Comment on the morphology of the red blood cells.
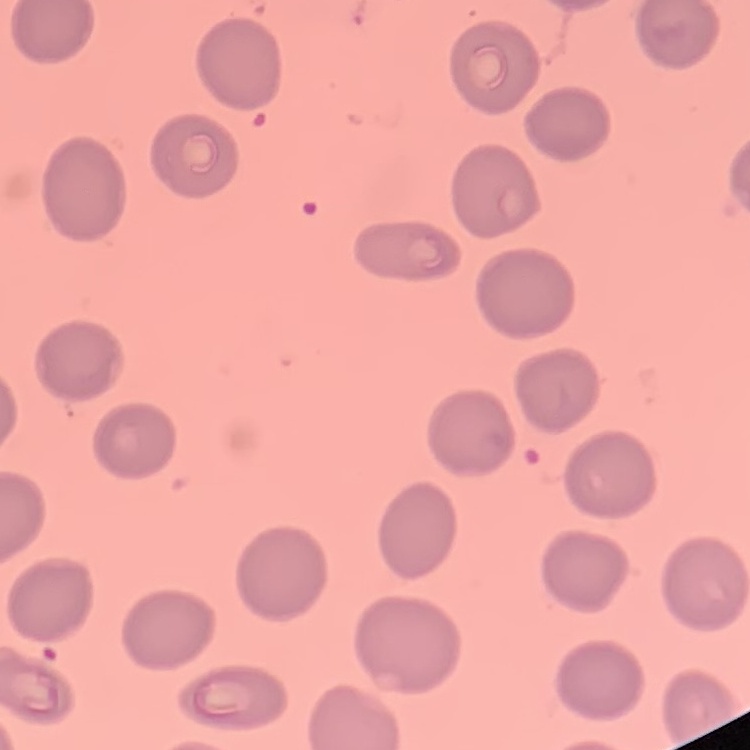

They show no rouleaux formation.

Summary:
  - Image type: square crop of a larger photomicrograph
  - Preparation: thin blood film
  - Stain: Field's or Giemsa